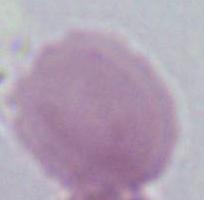

modality = micrograph
magnification = 1000x
identification = erythrocyte